Assess this cell for malaria.
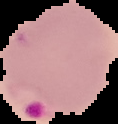

It is parasitized.

Summary:
  - Image size: 118×124 pixels
  - Preparation: thin blood smear
  - Image type: segmented cell region with the area outside set to black